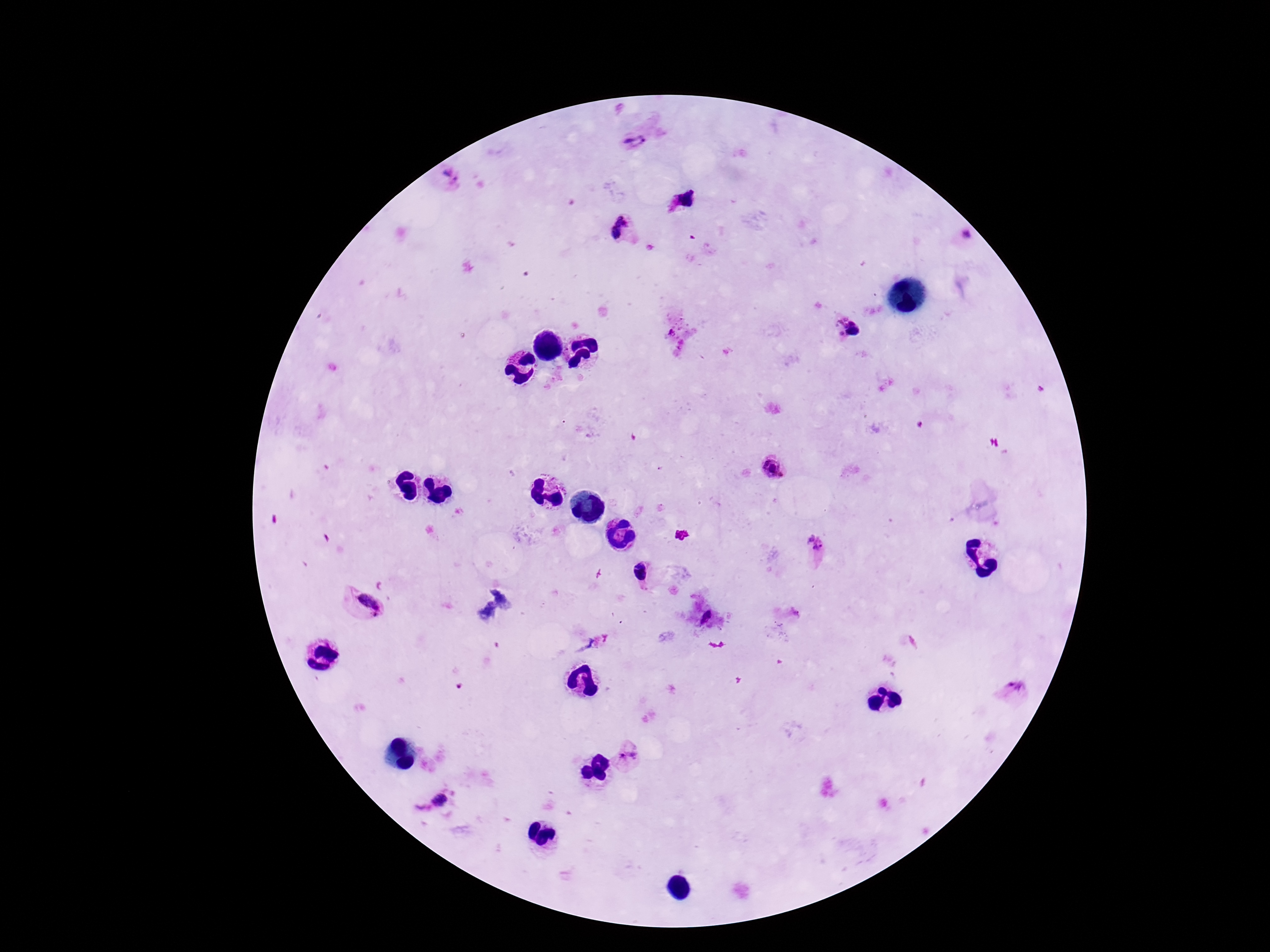

preparation = thick peripheral-blood smear
Plasmodium parasite locations = approximate centers as [x, y] in pixels: [632, 141], [447, 174], [686, 199], [620, 216], [620, 222], [616, 233], [968, 237], [839, 317], [852, 324], [845, 325], [842, 335], [854, 335], [772, 468], [815, 542], [640, 571], [371, 603], [706, 615], [1015, 686], [629, 757], [439, 801]
field of view = one from this slide
magnification = 100x
patient malaria status = infected
capture = smartphone camera through the microscope eyepiece
stain = Giemsa
image size = 1270×952 pixels